Outline each blood parasite and name the species.
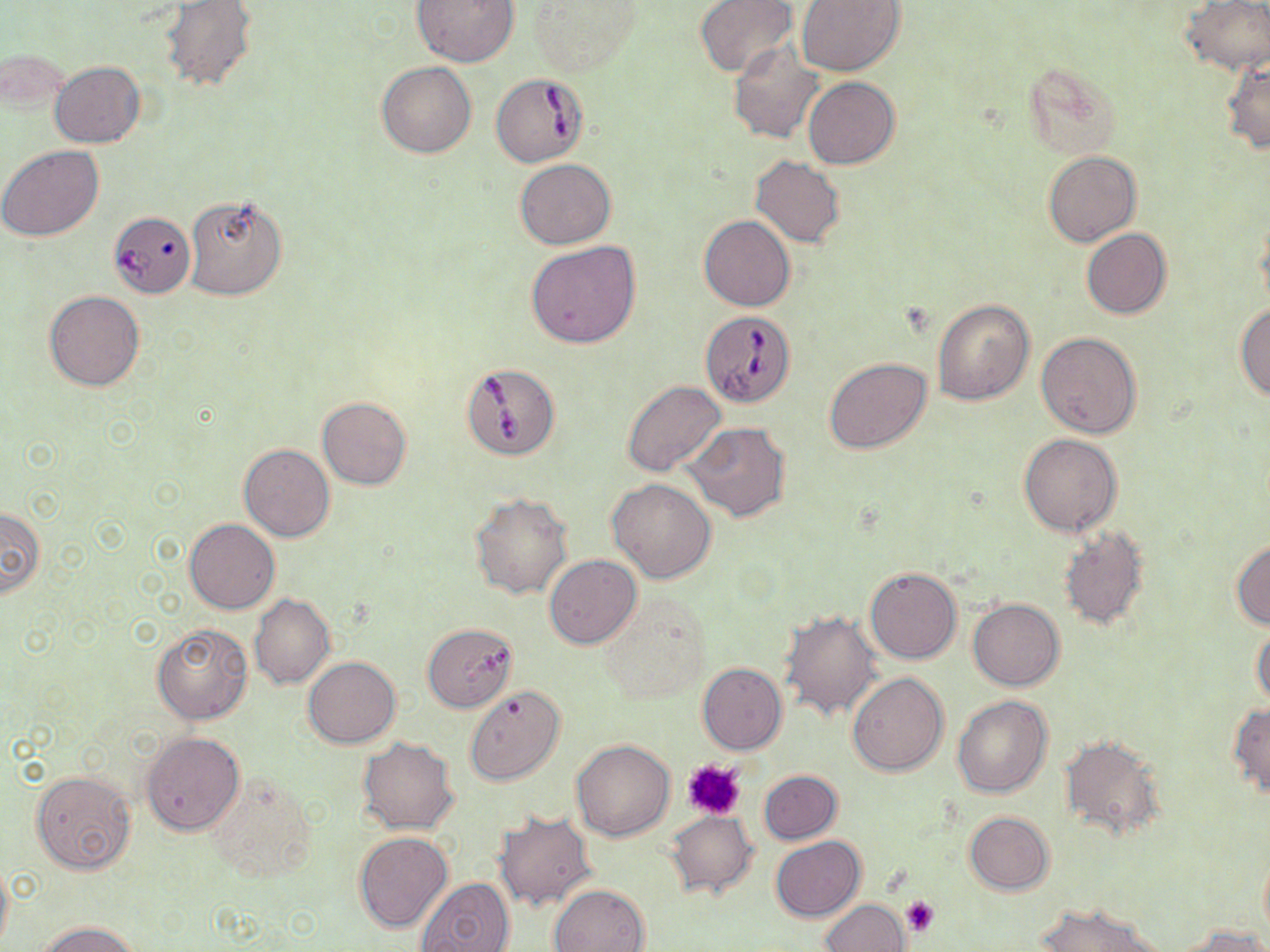

Approximate bounding boxes as (x1,y1)-(x2,y2) corner pairs in pixels.
Babesia divergens-infected red blood cells: (490,73)-(590,168), (107,211)-(194,304), (701,310)-(795,406), (461,363)-(562,460).
No Plasmodium falciparum, Plasmodium ovale, Plasmodium malariae, Plasmodium vivax, or Trypanosoma brucei observed.

Summary:
  - Uninfected red blood cell locations: (411,0)-(520,68), (695,0)-(797,78), (796,0)-(905,76), (1183,0)-(1270,75), (160,1)-(258,92), (527,1)-(642,75), (729,44)-(824,144), (0,46)-(70,116), (1222,56)-(1270,154), (50,60)-(145,148), (1019,60)-(1120,159), (377,61)-(476,158), (802,77)-(900,169), (0,145)-(104,243), (1043,151)-(1141,246), (751,156)-(845,247), (514,159)-(617,249), (183,192)-(287,301), (699,215)-(795,311), (1081,228)-(1172,319), (526,239)-(641,348), (44,291)-(145,391), (931,297)-(1034,405), (1235,303)-(1270,403), (1037,332)-(1142,439), (824,357)-(931,454), (623,381)-(726,477), (317,397)-(412,489), (685,422)-(790,521), (1018,433)-(1122,537), (238,444)-(334,542), (608,479)-(716,583), (469,491)-(572,599), (0,506)-(46,600), (184,519)-(279,613), (1057,528)-(1150,630), (1231,538)-(1270,630), (544,555)-(640,649), (864,566)-(962,664), (599,592)-(710,704), (249,593)-(335,689), (969,599)-(1064,691), (781,609)-(883,720), (151,622)-(252,724), (422,623)-(518,711), (1252,628)-(1270,708), (304,657)-(400,748), (697,663)-(786,755), (847,673)-(948,775), (464,685)-(564,784), (952,695)-(1052,798), (1228,703)-(1270,796), (143,732)-(244,836), (1060,734)-(1166,841), (357,738)-(458,834), (571,739)-(676,841), (759,769)-(842,844), (29,771)-(136,874), (205,776)-(318,886), (666,811)-(758,898), (964,811)-(1054,894), (495,813)-(596,910), (353,832)-(453,933), (770,836)-(865,921), (1259,851)-(1270,943), (0,857)-(12,952), (415,877)-(516,952), (549,882)-(650,951), (820,899)-(909,951), (1035,903)-(1166,952), (37,921)-(140,952), (1180,923)-(1266,952)
  - Platelet locations: (683,760)-(746,820), (902,896)-(940,938)
  - Slide-level diagnosis: Babesia divergens
  - Stain: May-Grünwald-Giemsa
  - Image size: 1270×952 pixels
  - Field of view: one of a larger specimen
  - Magnification: 1000x
  - Preparation: thin blood smear
  - Modality: optical microscopy